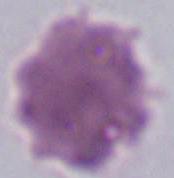
magnification = 1000x
modality = micrograph
identification = erythrocyte